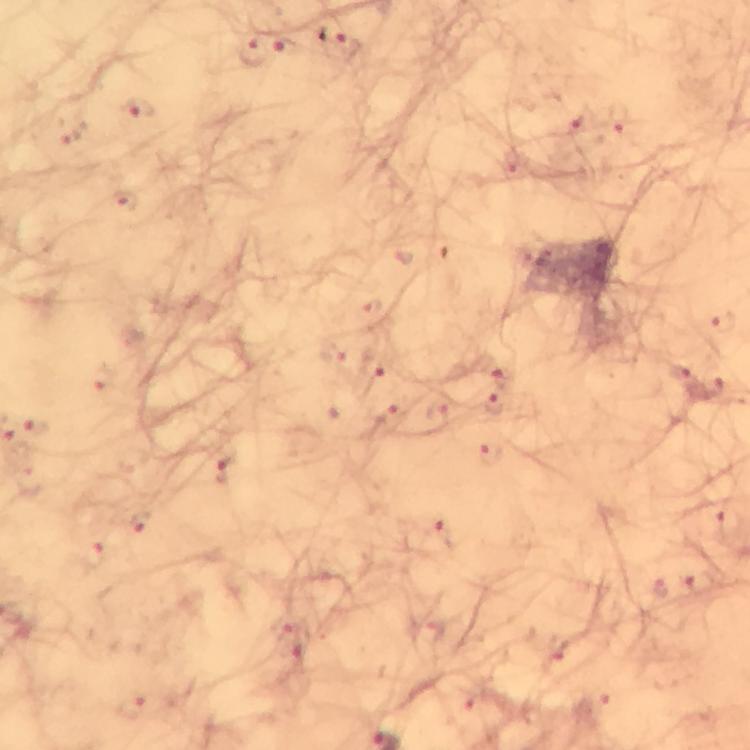
Approximate object centers, in pixels from the top-left corner.
Summary:
  - Plasmodium parasite locations: (x=338, y=44), (x=287, y=45), (x=253, y=53), (x=140, y=108), (x=493, y=406)
  - Image size: 750×750 pixels
  - Capture: smartphone camera through the microscope
  - Preparation: thick blood film
  - Immersion oil: applied
  - Stain: Giemsa
  - Context: from a malaria diagnostic workup
  - Magnification: 100x
  - Cropped from: a single field of view